State which parasite is depicted.
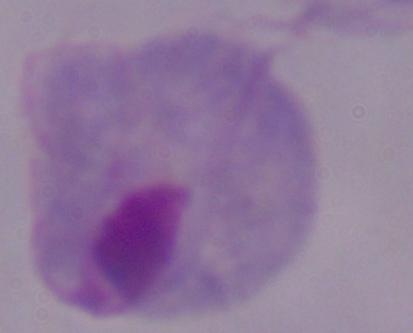

A trichomonad.

Captured at 1000x magnification. Micrograph.